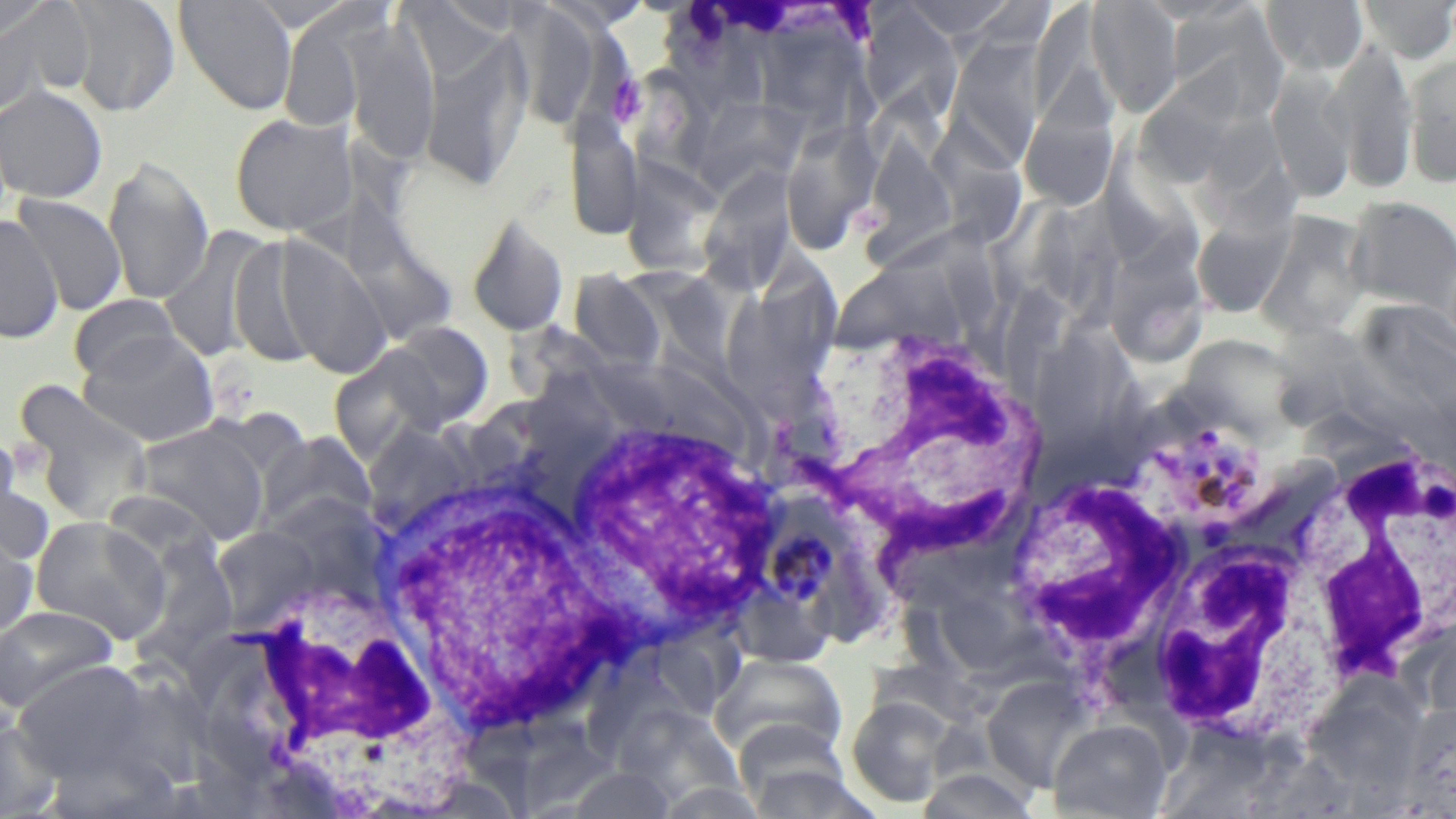
Summary:
  - Coordinate format: approximate bounding boxes as [x1, y1, x2, y2] in pixels
  - White blood cell locations: [802, 324, 1049, 581], [559, 412, 782, 639], [1291, 438, 1454, 686], [1000, 469, 1194, 686], [373, 480, 615, 744], [1142, 529, 1338, 747], [200, 575, 462, 803]
  - Uninfected red blood cell locations: [64, 0, 181, 117], [174, 0, 298, 116], [900, 0, 1018, 39], [1086, 0, 1184, 116], [1261, 0, 1367, 76], [1356, 0, 1456, 62], [0, 1, 55, 44], [506, 2, 605, 132], [0, 3, 91, 108], [400, 3, 506, 87], [1030, 3, 1111, 129], [1166, 4, 1288, 121], [859, 5, 963, 123], [278, 7, 377, 132], [760, 9, 889, 148], [665, 11, 778, 116], [343, 19, 441, 163], [420, 33, 531, 193], [944, 37, 1046, 168], [1327, 40, 1418, 193], [1404, 53, 1456, 186], [1136, 57, 1252, 187], [1266, 68, 1357, 205], [635, 69, 712, 191], [0, 85, 108, 203], [697, 90, 811, 199], [1018, 109, 1119, 212], [564, 111, 642, 243], [228, 112, 357, 238], [934, 114, 1022, 253], [781, 116, 883, 254], [861, 128, 957, 261], [1103, 133, 1196, 277], [102, 155, 214, 305], [698, 164, 799, 296], [623, 178, 731, 281], [12, 194, 128, 315], [332, 196, 461, 355], [1345, 196, 1456, 313], [1191, 209, 1295, 319], [1255, 210, 1372, 341], [465, 213, 570, 336], [1, 215, 63, 345], [1115, 219, 1219, 369], [162, 226, 275, 362], [271, 233, 390, 378], [227, 234, 332, 369], [662, 245, 765, 376], [757, 247, 842, 385], [838, 247, 971, 363], [567, 270, 666, 374], [724, 292, 835, 419], [69, 294, 183, 383], [379, 322, 494, 431], [507, 325, 619, 407], [1181, 328, 1319, 439], [78, 330, 220, 446], [15, 380, 155, 528], [371, 419, 475, 534], [133, 424, 269, 546], [258, 430, 378, 536], [0, 463, 54, 567], [29, 515, 170, 642], [212, 528, 318, 628], [0, 530, 39, 639], [135, 530, 236, 680], [938, 588, 1055, 671], [0, 605, 119, 712], [654, 621, 747, 719], [709, 653, 849, 763], [13, 659, 155, 781], [981, 675, 1098, 793], [619, 692, 751, 809], [846, 695, 955, 807], [1399, 700, 1455, 815], [0, 719, 63, 817], [1048, 719, 1172, 819], [743, 760, 879, 819], [914, 767, 1041, 819], [656, 781, 770, 818]
  - Platelet locations: [605, 74, 646, 125]
  - Plasmodium malariae-infected red blood cell locations: [1133, 411, 1273, 541], [761, 493, 857, 615]
  - Slide-level diagnosis: Plasmodium malariae
  - Preparation: thin blood film
  - Modality: optical microscopy
  - Magnification: 1000x
  - Stain: May-Grünwald-Giemsa
  - Image size: 1456×819 pixels
  - Field of view: single